Give the position of every leukocyte visible.
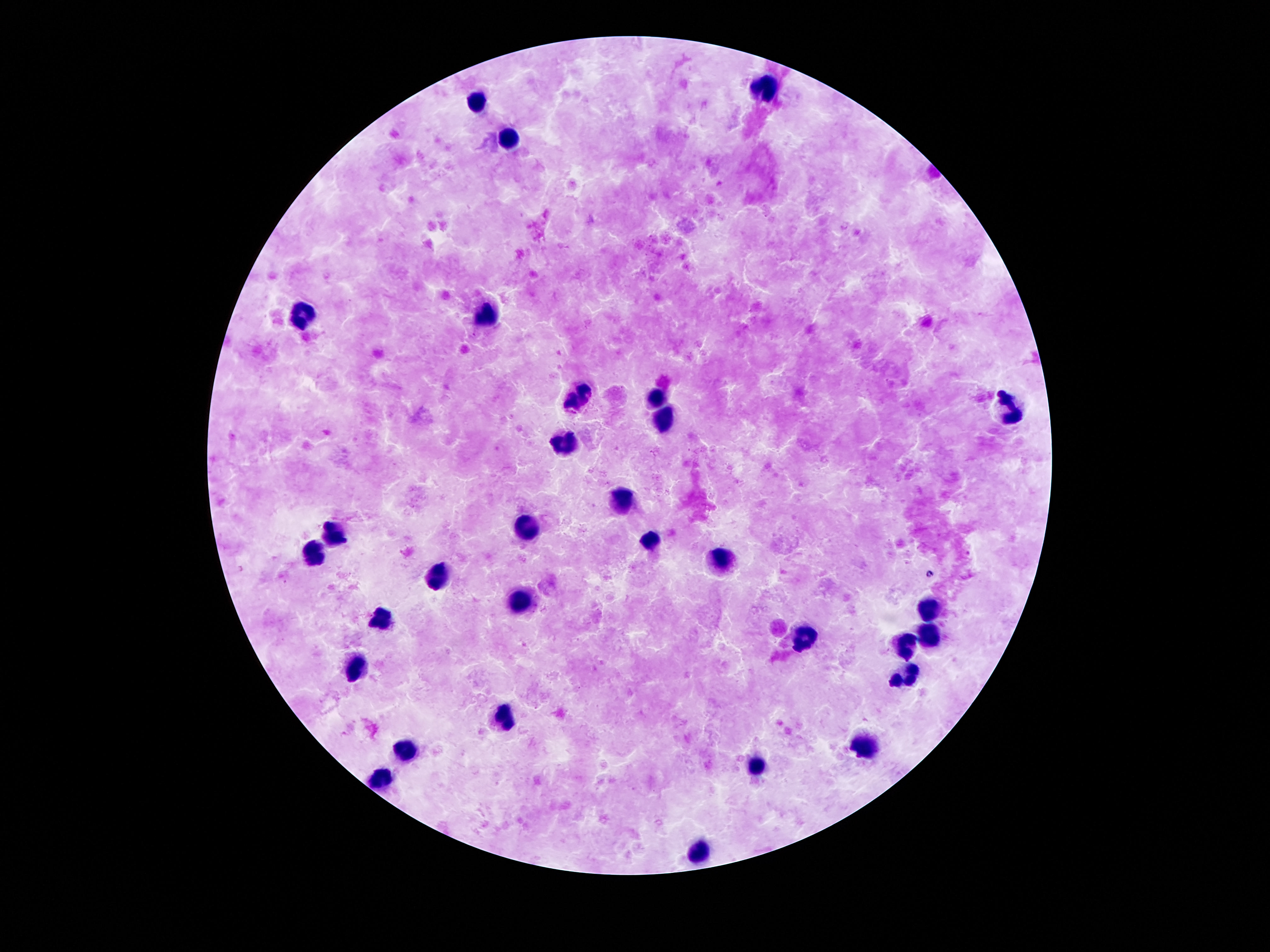
Approximate centers as {x, y} in pixels.
Leukocytes: {763, 88}, {478, 103}, {508, 139}, {307, 312}, {487, 317}, {579, 397}, {655, 397}, {1010, 411}, {666, 419}, {567, 443}, {623, 501}, {531, 527}, {335, 532}, {650, 542}, {317, 550}, {724, 560}, {437, 577}, {524, 600}, {928, 606}, {379, 621}, {931, 633}, {804, 636}, {907, 644}, {356, 669}, {905, 672}, {503, 715}, {865, 746}, {404, 750}, {760, 765}, {381, 778}, {699, 850}.

field of view = one from this slide
image size = 1270×952 pixels
magnification = 100x
stain = Giemsa
patient malaria status = not infected
preparation = thick blood smear
capture = smartphone camera through the microscope eyepiece